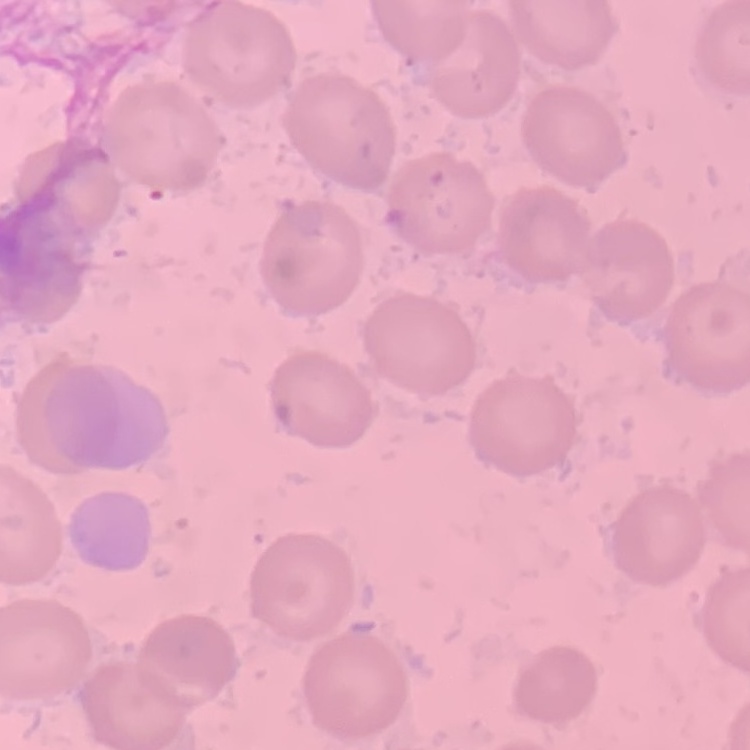

Summary:
  - Red blood cell morphology: no rouleaux formation
  - Preparation: thin blood film
  - Stain: Field's or Giemsa
  - Image type: one tile cut from a larger photomicrograph